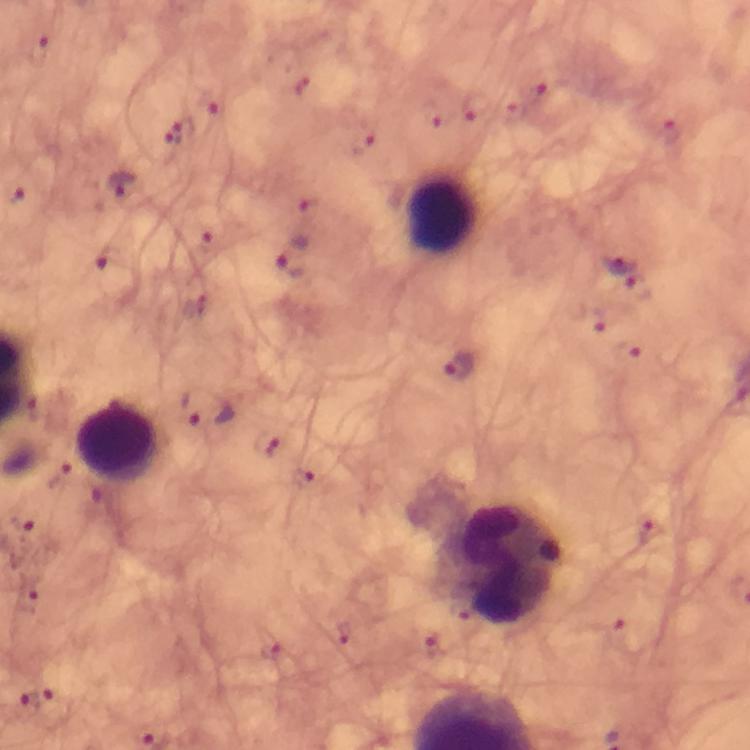

Approximate object centers, in pixels from the top-left corner. Malaria parasite locations: (x=38, y=51), (x=535, y=97), (x=475, y=105), (x=205, y=107), (x=178, y=132), (x=668, y=134), (x=365, y=142), (x=122, y=187), (x=295, y=257), (x=621, y=258), (x=114, y=270), (x=640, y=286), (x=460, y=369), (x=210, y=410), (x=269, y=443), (x=302, y=477), (x=27, y=523), (x=652, y=533), (x=28, y=597), (x=434, y=645), (x=273, y=652), (x=23, y=702), (x=53, y=709). Leukocyte locations: (x=442, y=215), (x=119, y=439), (x=507, y=565). At 100x magnification. Photographed with a smartphone mounted on the microscope. From a malaria diagnostic workup. Giemsa-stained preparation. A crop from one field of view. Immersion oil applied. Image is 750×750 pixels. Thick smear.